Assess the morphology of the red blood cells.
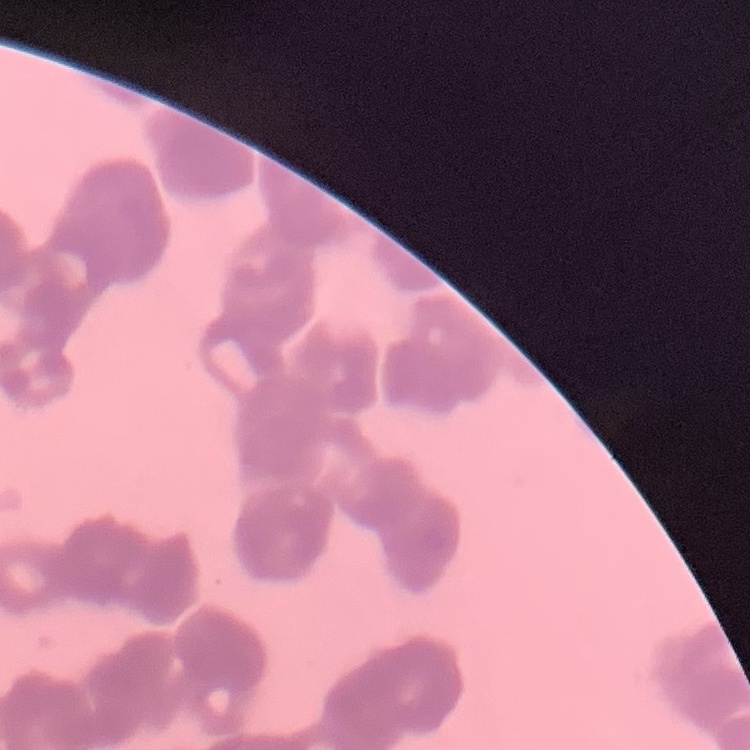

Rouleaux formation.

{
  "image_type": "one tile cut from a larger photomicrograph",
  "preparation": "thin peripheral smear",
  "stain": "Field's or Giemsa"
}